Assess this cell for malaria.
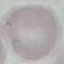

It is uninfected.

{
  "capture": "smartphone through the microscope eyepiece",
  "preparation": "thin blood smear",
  "stain": "Giemsa",
  "image_type": "cell patch, automatically extracted from a larger field of view and resized to 64 × 64 pixels"
}